State the blood parasite species.
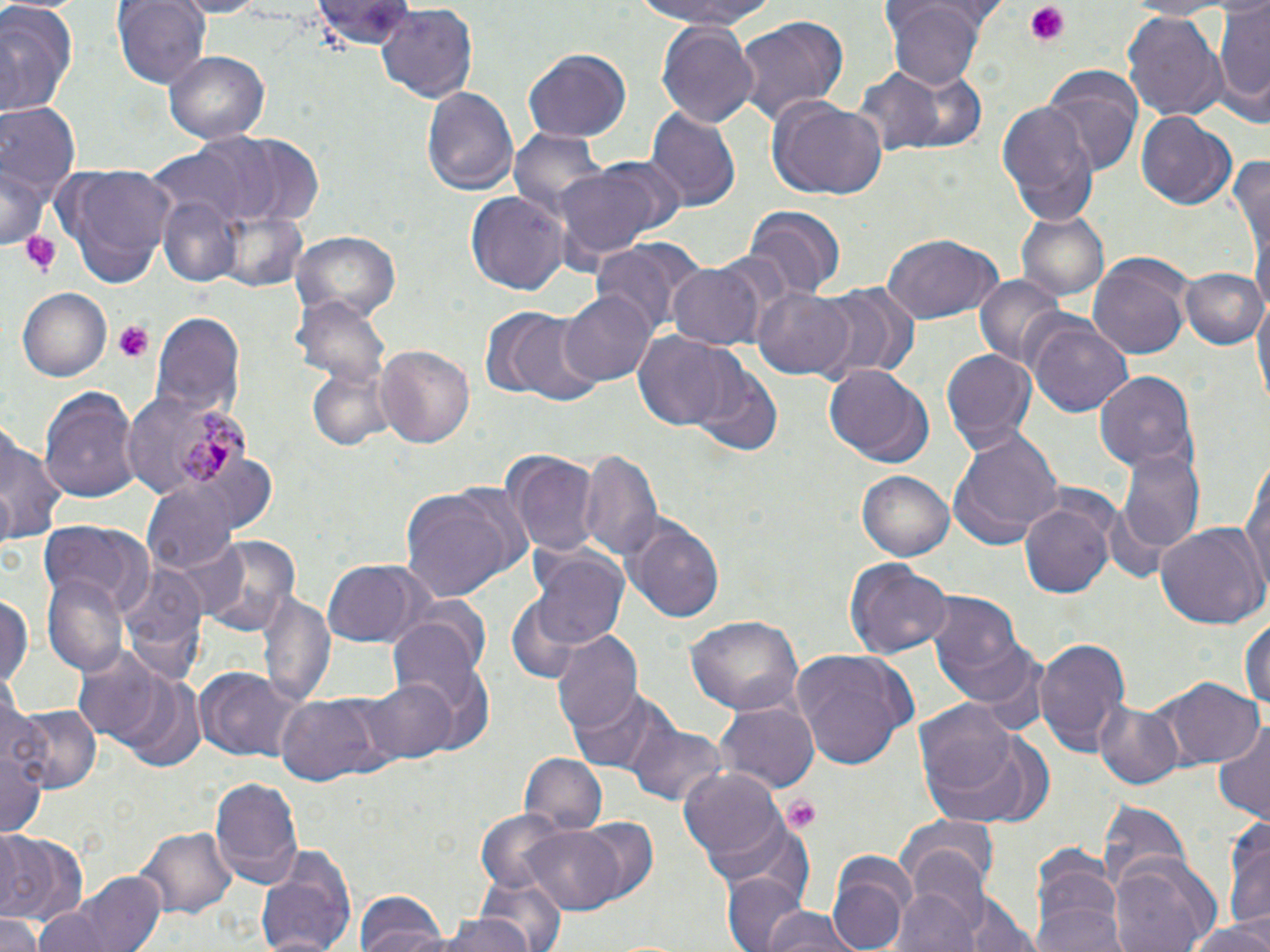
Plasmodium malariae.

Approximate bounding boxes as (x1, y1, x2, y2) in pixels. Platelet locations: (1023, 2, 1072, 48), (22, 229, 62, 277), (114, 321, 151, 362), (783, 795, 823, 831). Plasmodium malariae-infected red blood cell locations: (170, 409, 252, 486). Uninfected red blood cell locations: (111, 0, 213, 87), (314, 0, 414, 49), (635, 0, 777, 30), (1124, 0, 1239, 18), (886, 3, 986, 90), (1213, 3, 1270, 112), (0, 4, 80, 117), (374, 5, 477, 104), (1122, 10, 1227, 119), (733, 14, 849, 126), (657, 20, 760, 131), (522, 48, 631, 145), (165, 50, 269, 143), (853, 68, 943, 155), (884, 70, 989, 154), (1042, 70, 1139, 173), (421, 84, 518, 199), (766, 97, 889, 201), (0, 100, 78, 210), (995, 100, 1099, 225), (646, 104, 742, 214), (1135, 113, 1236, 211), (509, 127, 613, 232), (165, 129, 293, 227), (225, 134, 326, 226), (1230, 152, 1269, 265), (2, 156, 46, 253), (551, 160, 674, 265), (55, 164, 179, 287), (464, 190, 568, 295), (155, 193, 241, 289), (741, 203, 845, 301), (1017, 211, 1111, 305), (291, 231, 401, 323), (879, 232, 1003, 324), (590, 237, 700, 336), (1087, 252, 1194, 360), (669, 262, 766, 349), (1182, 265, 1267, 351), (973, 274, 1071, 372), (752, 282, 857, 379), (813, 282, 921, 383), (15, 287, 111, 382), (562, 290, 653, 387), (1254, 294, 1270, 406), (295, 297, 391, 391), (486, 306, 603, 407), (150, 308, 245, 420), (1025, 317, 1135, 418), (631, 332, 741, 432), (375, 345, 475, 447), (940, 346, 1037, 450), (823, 365, 934, 468), (692, 366, 782, 457), (1094, 368, 1199, 474), (309, 372, 393, 453), (40, 385, 139, 504), (0, 427, 67, 549), (951, 427, 1061, 545), (1118, 444, 1206, 557), (578, 445, 662, 562), (504, 450, 598, 559), (1240, 455, 1270, 592), (858, 468, 958, 561), (142, 481, 239, 575), (400, 484, 526, 600), (1020, 496, 1117, 599), (627, 517, 725, 623), (39, 522, 151, 613), (1155, 522, 1266, 630), (192, 535, 303, 640), (531, 549, 629, 652), (843, 557, 953, 658), (321, 558, 431, 646), (118, 560, 206, 679), (43, 574, 128, 677), (259, 590, 336, 708), (928, 592, 1031, 708), (0, 593, 31, 693), (506, 595, 589, 684), (1240, 610, 1269, 721), (384, 615, 492, 720), (685, 615, 805, 715), (550, 629, 644, 740), (1035, 637, 1131, 755), (72, 645, 164, 743), (789, 649, 916, 773), (197, 666, 294, 757), (107, 671, 207, 771), (360, 675, 454, 763), (1163, 676, 1262, 769), (569, 687, 679, 778), (278, 693, 390, 786), (1093, 698, 1184, 789), (916, 699, 1021, 801), (717, 700, 818, 793), (11, 703, 100, 794), (1214, 718, 1270, 822), (627, 720, 725, 806), (923, 729, 1056, 828), (1, 743, 46, 840), (518, 752, 607, 834), (680, 768, 788, 869), (209, 775, 305, 887), (1097, 798, 1191, 896), (473, 809, 576, 895), (702, 811, 817, 909), (1222, 814, 1270, 934), (568, 817, 659, 901), (894, 817, 1000, 892), (521, 823, 630, 913), (135, 826, 237, 918), (0, 830, 83, 926), (255, 845, 360, 952), (1030, 849, 1126, 952), (901, 851, 991, 938), (827, 854, 914, 950), (1108, 855, 1221, 952), (70, 873, 168, 951), (472, 873, 565, 947), (722, 874, 812, 952), (896, 886, 978, 952), (961, 893, 1040, 952), (357, 896, 451, 952), (33, 906, 111, 952), (754, 908, 860, 952), (0, 914, 43, 952), (433, 915, 542, 952), (1180, 916, 1270, 952). Thin blood smear. Captured at 1000x magnification. May-Grünwald-Giemsa-stained preparation. One field of a larger specimen. Optical microscopy. Image is 1270×952 pixels.